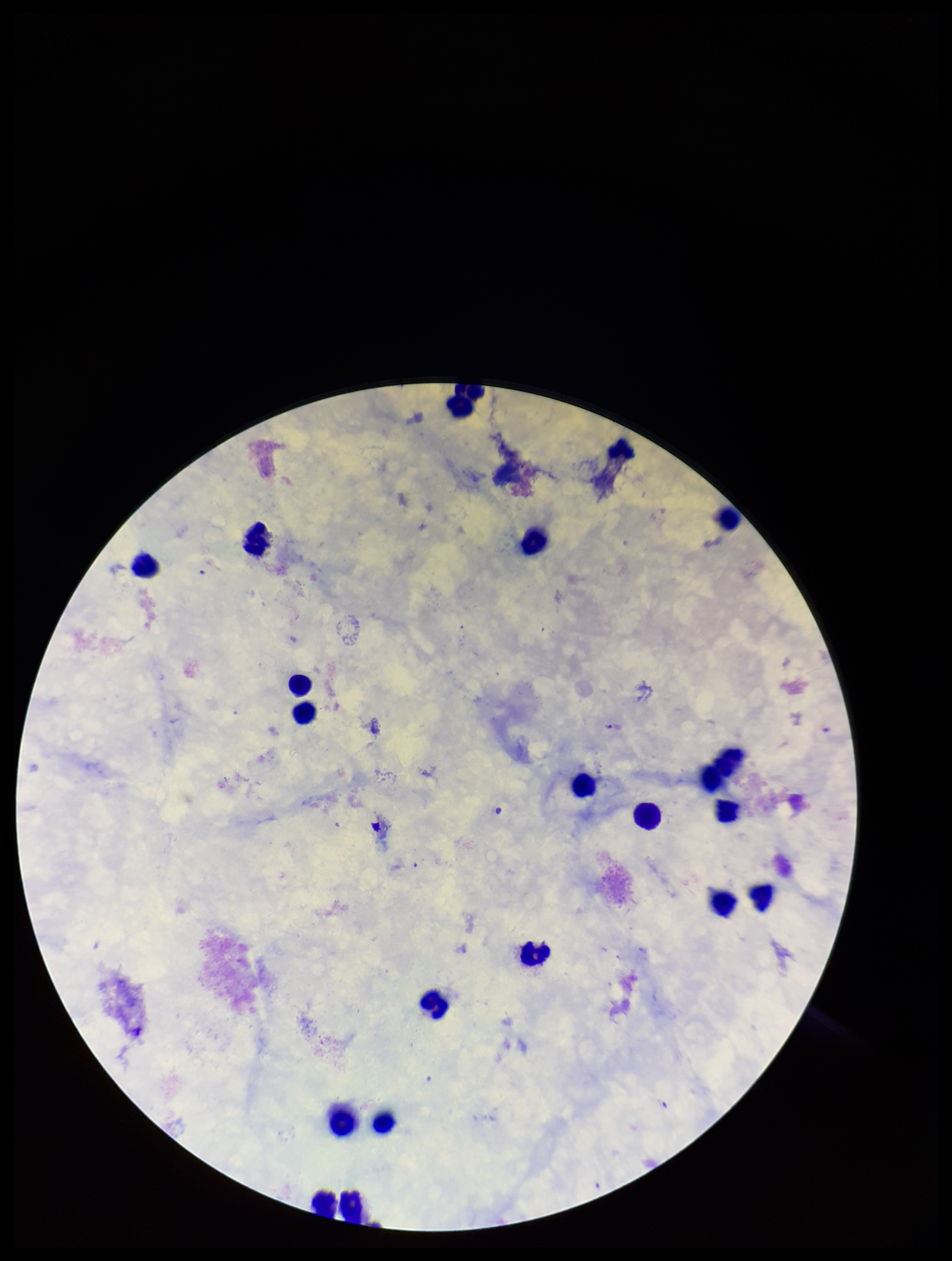

Plasmodium parasites = none detected
capture = smartphone photograph through the microscope eyepiece
stain = Giemsa
species reported for this patient = Plasmodium falciparum
preparation = thick blood smear
field of view = single
image size = 952×1261 pixels
leukocyte count = 20
parasite count = 0
patient malaria status = infected